Outline each Plasmodium malariae-infected red blood cell.
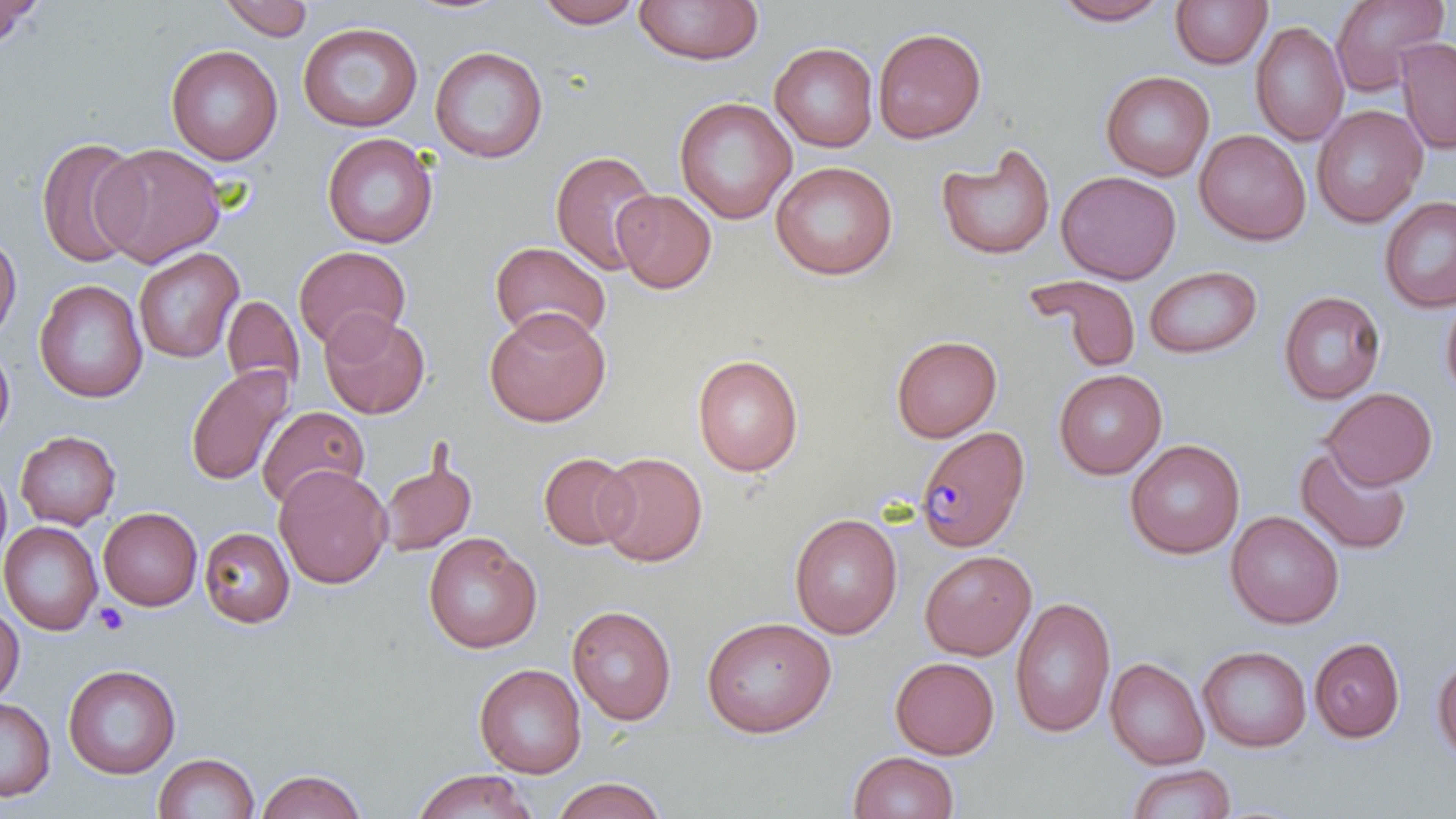

Approximate bounding boxes as [x1, y1, x2, y2] in pixels.
Plasmodium malariae-infected red blood cells: [916, 426, 1030, 552].

slide-level diagnosis = Plasmodium malariae
preparation = thin blood smear
image size = 1456×819 pixels
platelet locations = approximate bounding boxes as [x1, y1, x2, y2] in pixels: [93, 603, 129, 635]
magnification = 1000x
modality = optical microscopy
stain = May-Grünwald-Giemsa
uninfected red blood cell locations = approximate bounding boxes as [x1, y1, x2, y2] in pixels: [0, 0, 41, 50], [218, 0, 314, 41], [634, 0, 764, 65], [1052, 0, 1171, 26], [1329, 0, 1450, 96], [400, 1, 514, 18], [532, 1, 645, 28], [1170, 1, 1272, 69], [1250, 21, 1349, 146], [298, 22, 423, 133], [873, 26, 987, 144], [1395, 36, 1456, 155], [769, 42, 878, 152], [166, 45, 283, 165], [429, 45, 548, 163], [1101, 70, 1215, 181], [674, 96, 796, 224], [1311, 105, 1428, 228], [1194, 129, 1311, 245], [321, 132, 438, 249], [36, 138, 147, 268], [94, 142, 227, 267], [936, 144, 1057, 261], [550, 149, 660, 275], [770, 161, 898, 280], [1056, 170, 1180, 284], [612, 189, 717, 294], [1379, 196, 1456, 313], [0, 233, 21, 342], [489, 241, 611, 345], [293, 245, 411, 351], [132, 247, 244, 364], [1144, 265, 1263, 359], [1025, 274, 1143, 374], [34, 279, 148, 403], [1278, 290, 1386, 405], [1440, 292, 1456, 402], [222, 295, 304, 394], [483, 307, 611, 427], [319, 309, 431, 419], [890, 334, 1002, 442], [0, 340, 15, 446], [692, 353, 803, 477], [185, 365, 295, 486], [1053, 368, 1167, 479], [1322, 387, 1438, 490], [257, 405, 370, 509], [15, 430, 121, 529], [1125, 439, 1245, 559], [1295, 444, 1412, 556], [538, 452, 638, 550], [594, 452, 707, 567], [377, 455, 478, 556], [0, 462, 12, 571], [274, 464, 392, 589], [98, 507, 202, 611], [1225, 510, 1344, 630], [789, 513, 902, 639], [0, 520, 103, 635], [199, 526, 296, 628], [423, 532, 542, 653], [919, 550, 1036, 660], [1010, 595, 1116, 738], [0, 605, 24, 704], [567, 605, 677, 725], [701, 615, 836, 738], [1309, 636, 1406, 743], [1198, 645, 1312, 752], [1431, 653, 1456, 763], [890, 656, 999, 759], [1105, 657, 1209, 770], [63, 663, 182, 779], [474, 663, 587, 778], [0, 697, 56, 802], [848, 751, 959, 819], [153, 752, 260, 819], [1126, 763, 1236, 819], [256, 769, 367, 819], [411, 769, 539, 819], [550, 777, 668, 818]
field of view = one of a larger specimen